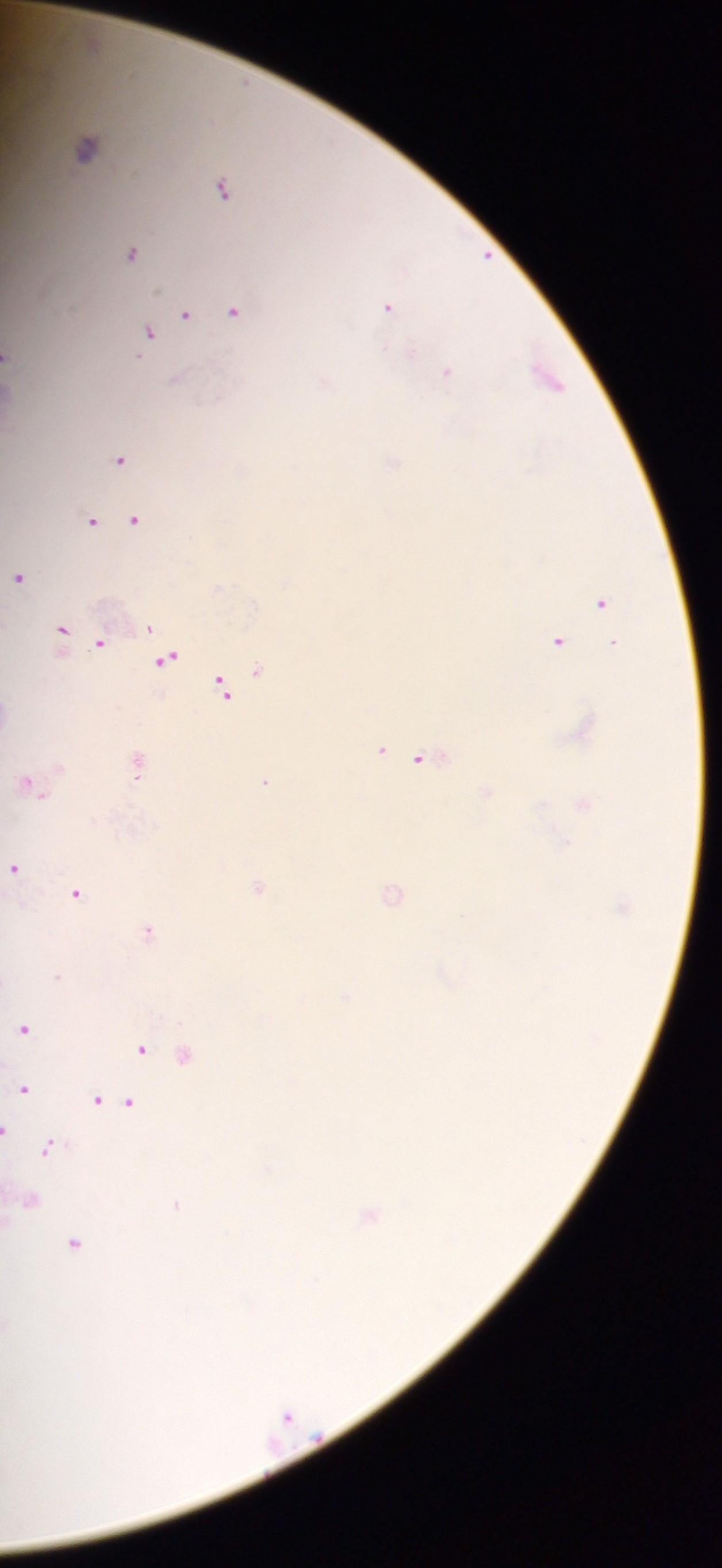

Approximate centers as (x, y) in pixels.
Summary:
  - Plasmodium parasite locations: (86, 148), (221, 187), (130, 252), (387, 307), (233, 310), (185, 314), (148, 332), (410, 353), (7, 355), (446, 372), (546, 377), (176, 378), (119, 458), (393, 464), (134, 519), (92, 520), (18, 577), (601, 602), (148, 627), (60, 631), (99, 641), (557, 641), (613, 643), (166, 659), (256, 669), (222, 687), (379, 750), (421, 760), (136, 764), (265, 782), (27, 783), (14, 869), (257, 888), (75, 893), (391, 894), (147, 930), (57, 977), (24, 1028), (140, 1048), (184, 1054), (23, 1090), (96, 1100), (128, 1102), (6, 1130), (47, 1148), (29, 1200), (176, 1204), (368, 1216), (74, 1243), (8, 1323)
  - Capture: mobile-phone photograph through a microscope
  - Preparation: thick blood film
  - Image size: 722×1568 pixels
  - Country: Ghana
  - Field of view: single